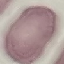

result = no malaria parasites seen
preparation = thin smear
stain = Giemsa
image type = cell patch, automatically extracted from a larger field of view and resized to 64 × 64 pixels
capture = smartphone through the microscope eyepiece